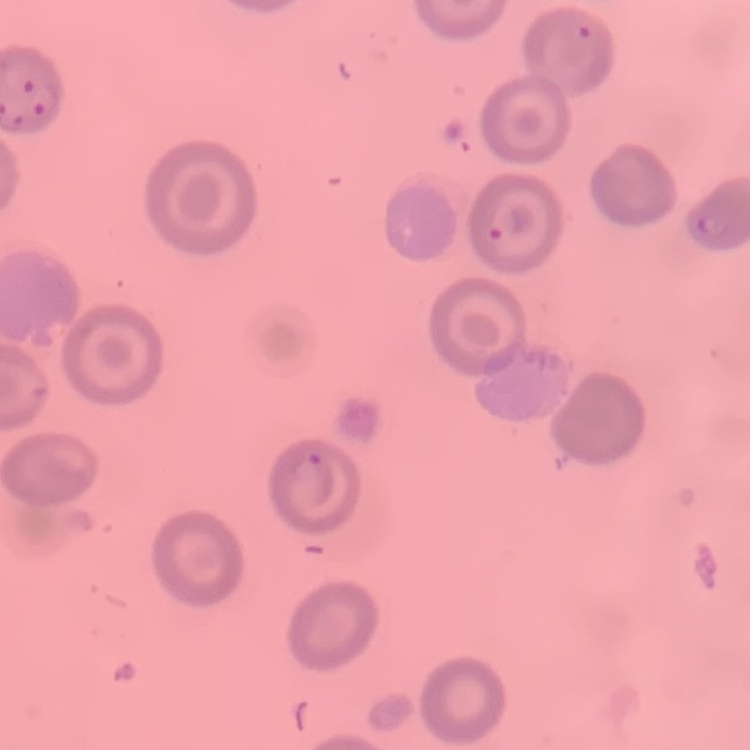
Summary:
  - Erythrocyte morphology: no rouleaux formation
  - Stain: Field's or Giemsa
  - Image type: square crop of a larger photomicrograph
  - Preparation: thin peripheral smear